Name the parasite shown.
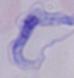
This is a trypanosome.

Captured at 1000x magnification. Photomicrograph.